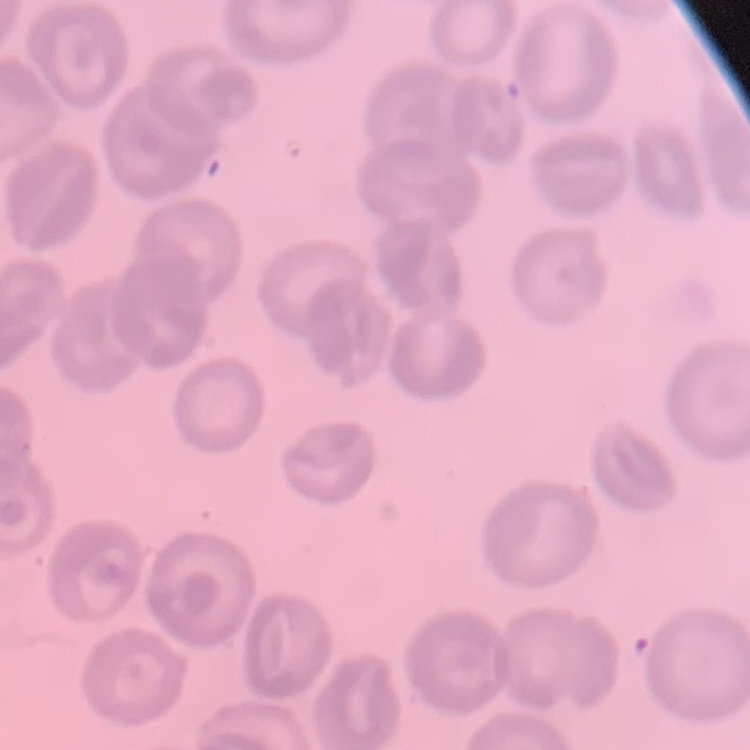

Summary:
  - Red blood cell morphology: no rouleaux formation
  - Image type: one tile cut from a larger photomicrograph
  - Preparation: thin peripheral smear
  - Stain: Field's or Giemsa